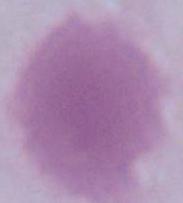
magnification = 1000x
identification = red blood cell
modality = micrograph